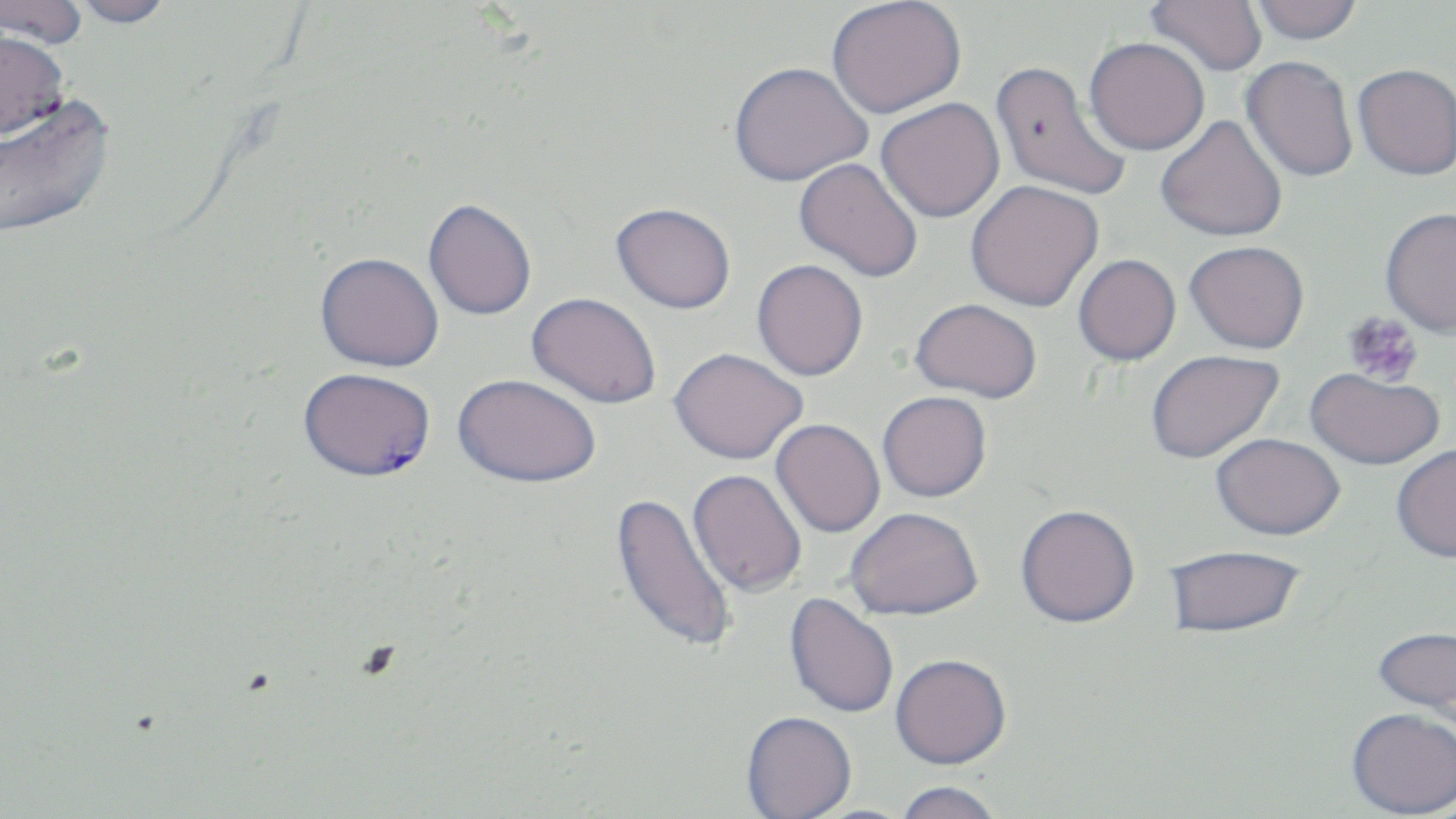
Summary:
  - Coordinate format: approximate bounding boxes as (x1,y1)-(x2,y2) corner pairs in pixels
  - Plasmodium falciparum-infected red blood cell locations: (299,367)-(436,481)
  - Platelet locations: (1342,311)-(1424,387)
  - Uninfected red blood cell locations: (0,0)-(89,49), (64,0)-(177,28), (827,0)-(966,118), (1146,0)-(1268,76), (1249,0)-(1364,44), (0,28)-(69,139), (1084,36)-(1210,155), (1241,56)-(1358,181), (990,60)-(1132,203), (729,62)-(872,186), (1353,63)-(1455,180), (0,92)-(116,240), (876,98)-(1005,223), (1156,115)-(1288,242), (794,158)-(924,282), (966,180)-(1104,311), (423,199)-(537,320), (611,202)-(736,313), (1380,206)-(1456,337), (1185,240)-(1310,353), (315,252)-(444,372), (1073,254)-(1181,366), (752,259)-(868,381), (527,292)-(662,408), (910,297)-(1043,402), (670,347)-(807,463), (1146,349)-(1284,463), (1305,368)-(1445,470), (453,373)-(601,487), (878,391)-(991,501), (771,418)-(886,537), (1211,432)-(1346,539), (1391,444)-(1456,562), (688,468)-(807,597), (611,491)-(739,655), (1016,504)-(1140,627), (845,506)-(984,620), (1163,544)-(1307,638), (784,592)-(899,718), (1371,624)-(1455,719), (890,653)-(1011,769), (1346,706)-(1456,817), (741,710)-(857,818), (894,780)-(1003,819)
  - Slide-level diagnosis: Plasmodium falciparum
  - Field of view: single
  - Image size: 1456×819 pixels
  - Stain: May-Grünwald-Giemsa
  - Preparation: thin blood smear
  - Magnification: 1000x
  - Modality: light microscopy